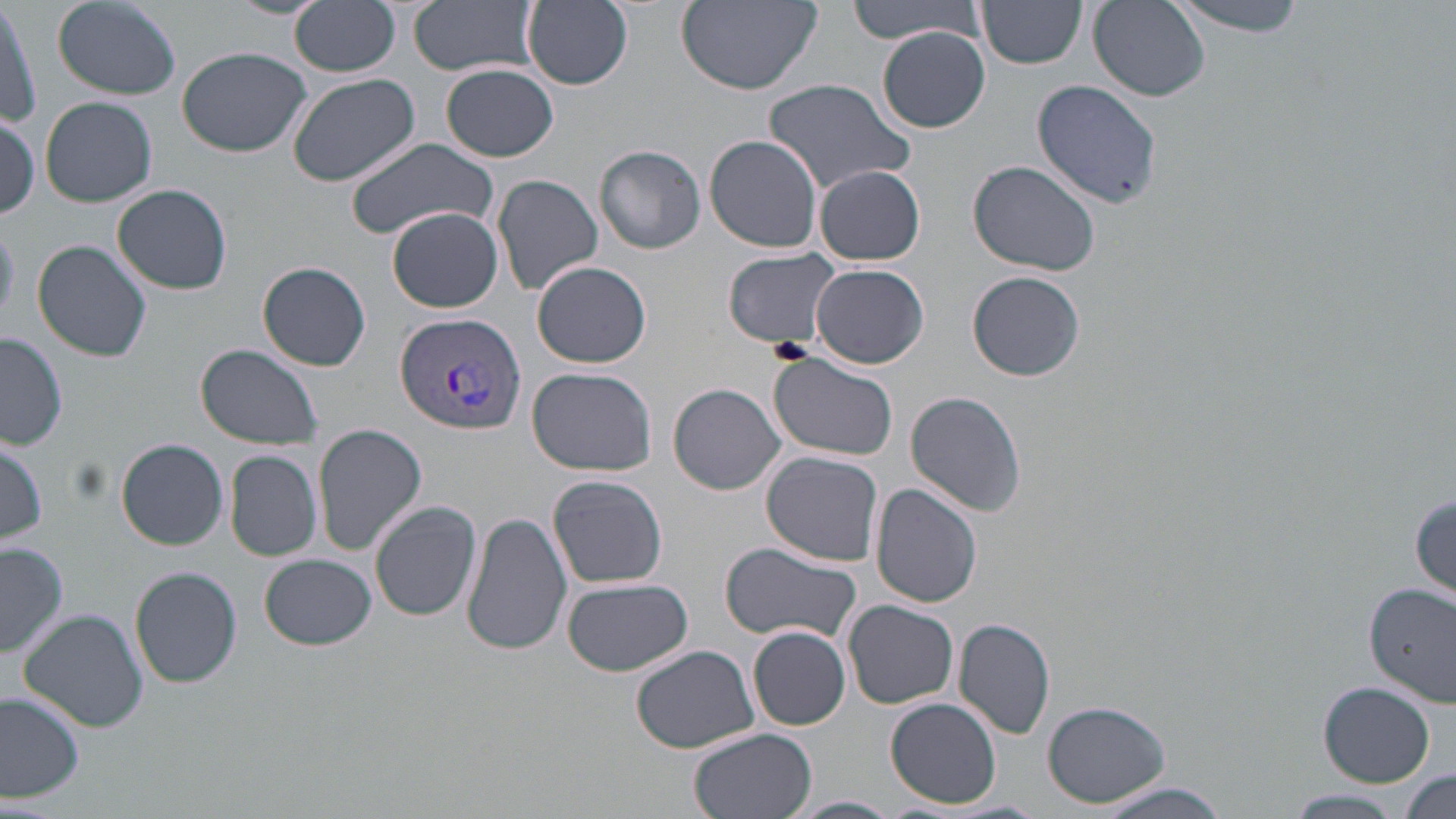
Approximate bounding boxes as [x1, y1, x2, y2] in pixels. Uninfected red blood cell locations: [229, 0, 326, 21], [289, 0, 402, 77], [411, 0, 538, 77], [522, 0, 634, 90], [674, 0, 825, 94], [849, 0, 986, 45], [975, 0, 1089, 69], [1170, 0, 1309, 36], [1, 1, 39, 130], [52, 1, 181, 99], [1088, 1, 1210, 101], [878, 28, 990, 133], [176, 47, 314, 158], [442, 63, 559, 162], [286, 72, 423, 187], [763, 78, 916, 196], [1031, 79, 1165, 210], [40, 97, 157, 208], [0, 113, 41, 219], [705, 134, 824, 254], [345, 139, 500, 241], [595, 145, 706, 252], [968, 161, 1101, 276], [815, 166, 925, 266], [493, 173, 605, 297], [113, 184, 233, 293], [387, 206, 504, 312], [32, 239, 152, 361], [724, 249, 841, 349], [532, 260, 653, 369], [259, 261, 370, 371], [812, 263, 929, 368], [967, 271, 1085, 381], [1, 332, 69, 451], [195, 344, 323, 450], [768, 353, 898, 461], [528, 366, 657, 476], [669, 382, 785, 495], [906, 392, 1026, 516], [313, 424, 427, 555], [0, 436, 47, 549], [117, 438, 229, 549], [225, 449, 321, 561], [761, 450, 885, 566], [549, 474, 668, 589], [872, 483, 984, 608], [1411, 490, 1455, 601], [370, 500, 483, 621], [462, 508, 572, 658], [1, 542, 68, 661], [717, 543, 865, 649], [260, 554, 377, 650], [129, 567, 242, 688], [560, 577, 694, 677], [1364, 580, 1456, 706], [844, 601, 959, 708], [20, 610, 149, 732], [954, 617, 1056, 739], [749, 625, 851, 730], [630, 646, 760, 755], [1318, 682, 1436, 787], [0, 693, 83, 804], [885, 697, 1002, 808], [1042, 699, 1171, 808], [686, 727, 818, 819], [1399, 769, 1454, 817], [1092, 783, 1233, 817], [1283, 790, 1404, 819], [789, 795, 902, 819]. Plasmodium vivax-infected red blood cell locations: [395, 312, 524, 434]. Slide-level diagnosis: Plasmodium vivax. Optical microscopy. One field of a larger specimen. Image is 1456×819 pixels. Captured at 1000x magnification. Thin blood smear. May-Grünwald-Giemsa stain.